Assess this cell for malaria.
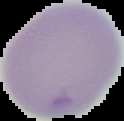
Uninfected.

image type = segmented cell region with the area outside set to black
image size = 124×121 pixels
preparation = thin blood smear